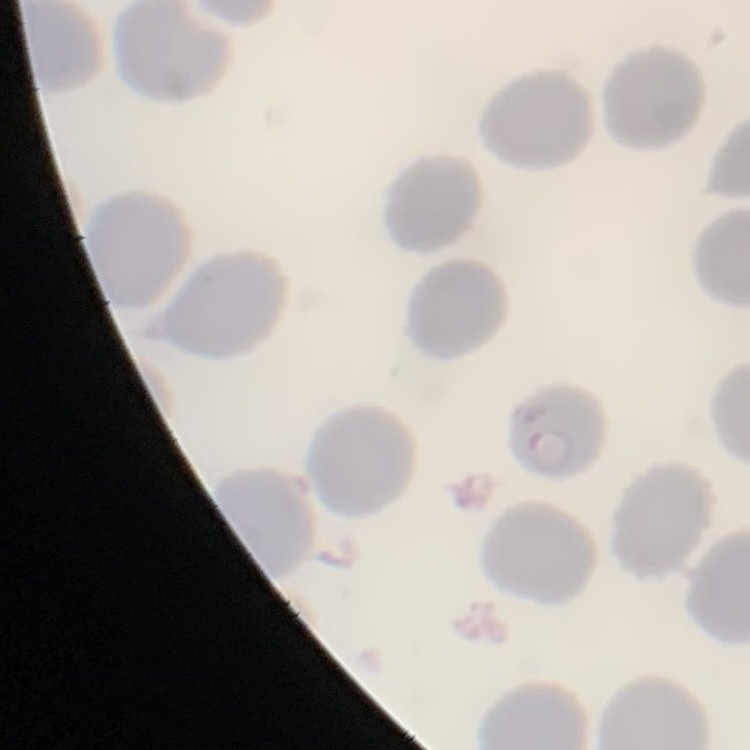

{
  "red_blood_cell_morphology": "no rouleaux formation",
  "stain": "Field's or Giemsa",
  "preparation": "thin blood smear",
  "image_type": "one tile cut from a larger photomicrograph"
}